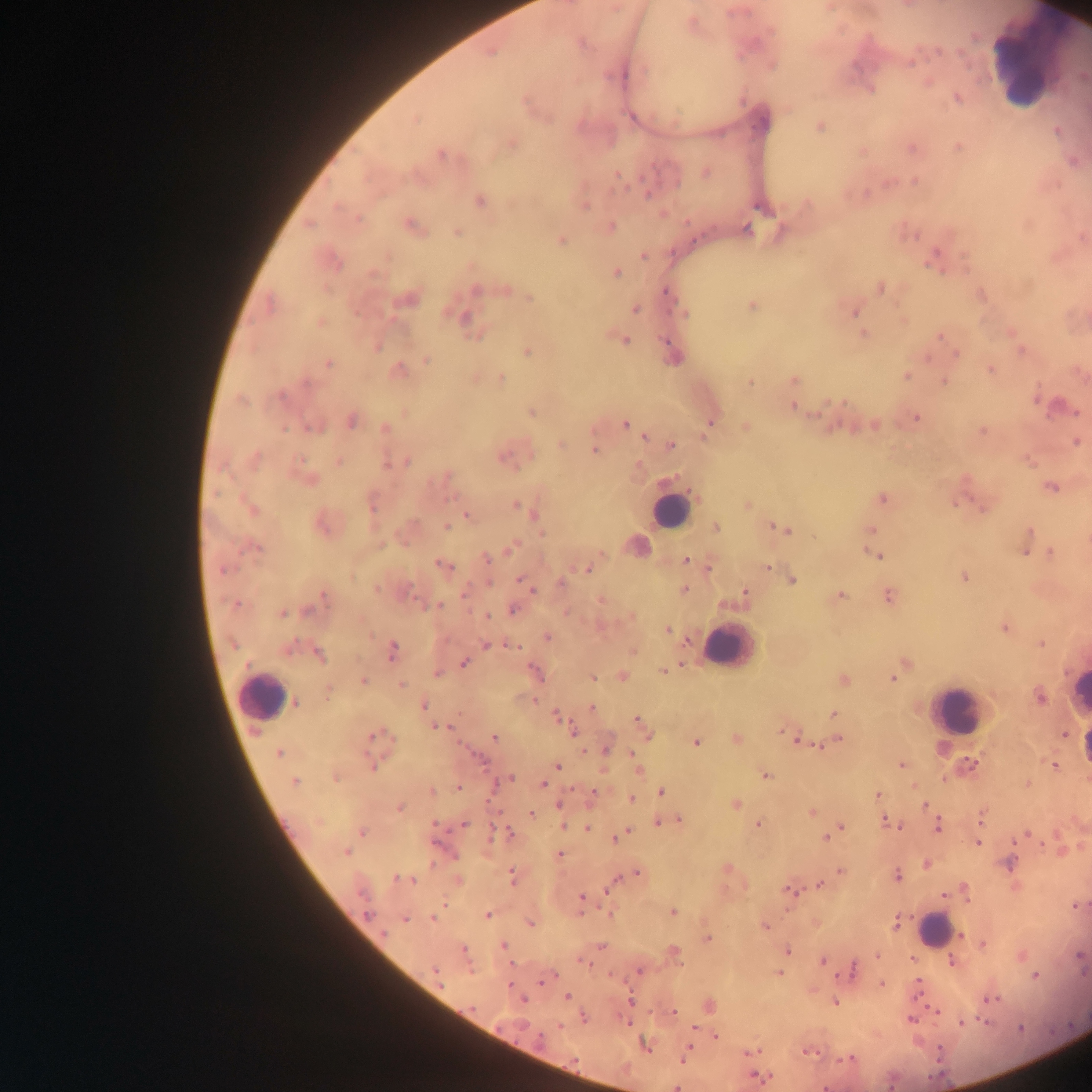
Approximate centers as [x, y] in pixels. Leukocyte locations: [1026, 68], [670, 510], [728, 646], [262, 694], [1078, 700], [956, 711], [932, 930]. Plasmodium parasite locations: [691, 23], [912, 61], [772, 66], [624, 75], [871, 90], [958, 98], [632, 117], [415, 120], [820, 128], [1057, 131], [510, 145], [958, 147], [911, 149], [863, 151], [441, 155], [706, 173], [617, 177], [915, 181], [647, 193], [481, 202], [585, 205], [761, 207], [359, 220], [310, 225], [411, 226], [611, 226], [747, 229], [457, 233], [561, 241], [644, 256], [934, 259], [335, 262], [617, 274], [374, 275], [881, 288], [477, 290], [505, 290], [667, 292], [981, 295], [530, 298], [411, 300], [270, 305], [752, 306], [635, 310], [854, 311], [685, 313], [462, 317], [321, 323], [864, 335], [941, 336], [625, 340], [378, 347], [1021, 351], [528, 352], [956, 354], [427, 360], [329, 363], [991, 369], [398, 370], [907, 376], [501, 378], [795, 380], [750, 382], [945, 382], [307, 384], [281, 395], [242, 401], [794, 407], [1069, 409], [531, 412], [915, 418], [352, 421], [625, 424], [746, 426], [874, 426], [708, 428], [285, 429], [313, 429], [386, 429], [982, 431], [705, 435], [645, 436], [1076, 442], [562, 444], [671, 445], [594, 451], [504, 458], [255, 459], [339, 462], [407, 462], [387, 464], [447, 477], [310, 480], [1051, 487], [883, 499], [958, 503], [747, 504], [372, 505], [515, 505], [981, 508], [251, 509], [522, 509], [467, 515], [535, 515], [324, 525], [446, 526], [716, 527], [782, 529], [871, 529], [1029, 532], [637, 547], [512, 548], [256, 549], [1026, 551], [1051, 552], [874, 554], [487, 559], [686, 560], [444, 566], [767, 567], [588, 568], [224, 570], [964, 577], [521, 580], [792, 580], [489, 583], [562, 584], [377, 588], [530, 588], [685, 590], [464, 594], [745, 595], [323, 596], [840, 596], [888, 597], [602, 600], [235, 604], [437, 606], [513, 610], [309, 611], [282, 613], [486, 616], [1004, 628], [667, 629], [548, 637], [1041, 643], [486, 644], [513, 647], [393, 651], [319, 655], [464, 662], [905, 663], [663, 670], [536, 673], [437, 674], [622, 676], [593, 677], [893, 679], [363, 681], [844, 681], [402, 685], [328, 694], [1040, 697], [296, 702], [424, 706], [592, 707], [557, 715], [834, 715], [637, 720], [438, 728], [572, 730], [785, 733], [373, 735], [649, 735], [494, 737], [736, 739], [838, 739], [799, 741], [696, 742], [606, 749], [279, 753], [972, 764], [902, 765], [1054, 765], [373, 766], [558, 766], [638, 771], [765, 776], [336, 779], [508, 780], [295, 781], [543, 784], [1027, 784], [458, 786], [431, 792], [594, 792], [662, 792], [878, 795], [632, 798], [735, 804], [559, 805], [925, 805], [401, 807], [811, 812], [531, 813], [981, 816], [679, 819], [885, 820], [661, 823], [435, 825], [464, 825], [564, 825], [758, 825], [938, 826], [587, 828], [840, 828], [835, 831], [362, 832], [507, 834], [1027, 834], [622, 835], [826, 837], [616, 838], [978, 843], [346, 852], [560, 854], [1008, 863], [926, 864], [728, 867], [841, 872], [637, 873], [512, 875], [897, 876], [398, 879], [409, 879], [458, 880], [821, 885], [611, 888], [789, 891], [946, 895], [582, 897], [1076, 906], [673, 913], [368, 914], [610, 914], [487, 915], [434, 918], [405, 919], [531, 923], [896, 923], [765, 926], [384, 934], [961, 935], [708, 938], [984, 944], [504, 946], [602, 947], [464, 949], [788, 950], [676, 955], [877, 956], [1079, 956], [584, 962], [678, 962], [822, 962], [952, 962], [435, 970], [639, 971], [852, 971], [779, 973], [1036, 976], [548, 978], [882, 984], [918, 984], [567, 996], [990, 998], [522, 1000], [630, 1001], [835, 1003], [674, 1011], [584, 1018], [911, 1019], [962, 1022], [559, 1027], [694, 1028], [1020, 1028], [717, 1036], [539, 1039], [646, 1046], [752, 1052], [808, 1052], [683, 1059], [848, 1059], [574, 1060], [760, 1077], [825, 1087], [676, 1088]. Image is 1092×1092 pixels. Thick blood film. One field of view. Collected in Ghana. Photographed through a microscope with a mobile-phone camera.